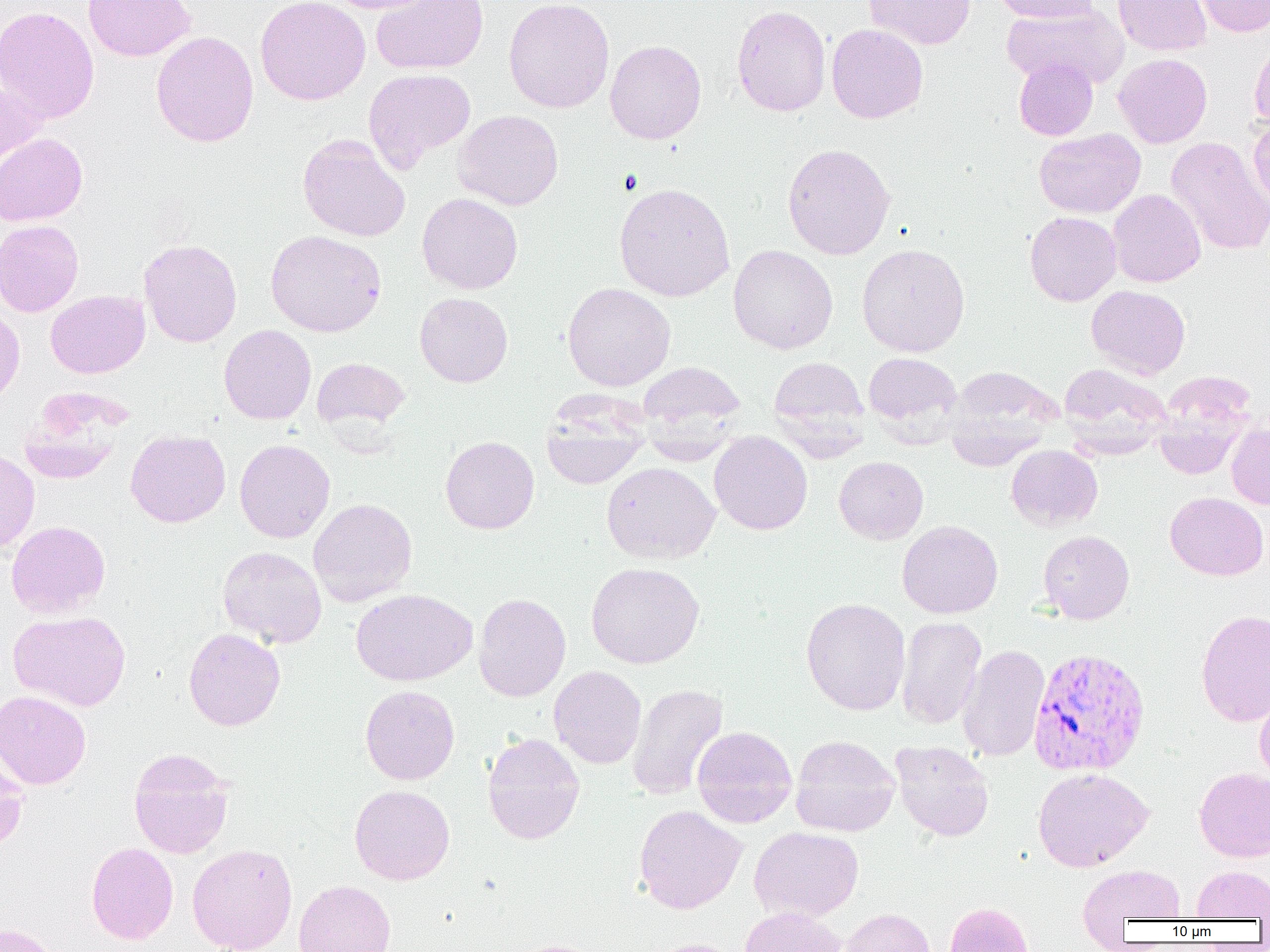

slide_level_diagnosis: Plasmodium vivax
uninfected_red_blood_cell_locations: 'approximate bounding boxes as (x1, y1, x2, y2) in pixels: (83, 0, 195, 62), (256, 0, 370, 105), (322, 0, 439, 14), (370, 0, 489, 75), (503, 0, 615, 113), (864, 0, 976, 50), (991, 0, 1099, 23), (1113, 0, 1211, 56), (1196, 0, 1269, 38), (1000, 3, 1129, 90), (732, 4, 831, 117), (0, 6, 100, 123), (826, 23, 928, 123), (151, 30, 259, 148), (1249, 37, 1270, 130), (605, 40, 706, 144), (1113, 53, 1212, 148), (1014, 57, 1098, 140), (363, 68, 476, 170), (0, 80, 46, 176), (453, 109, 564, 210), (1248, 118, 1270, 211), (1035, 128, 1146, 218), (0, 133, 87, 226), (297, 133, 411, 242), (1166, 137, 1270, 256), (782, 142, 896, 260), (613, 182, 735, 302), (1108, 189, 1206, 287), (417, 193, 523, 294), (1024, 211, 1121, 306), (0, 220, 84, 317), (265, 230, 386, 337), (138, 238, 242, 347), (857, 242, 970, 357), (728, 244, 838, 354), (562, 281, 676, 390), (1086, 284, 1191, 378), (45, 290, 150, 378), (414, 292, 513, 387), (0, 303, 25, 406), (219, 324, 316, 424), (863, 351, 962, 432), (768, 356, 869, 442), (312, 357, 410, 433), (636, 361, 745, 436), (1058, 362, 1172, 454), (944, 365, 1063, 464), (1154, 378, 1253, 479), (18, 396, 127, 486), (541, 421, 649, 490), (1226, 422, 1270, 509), (125, 429, 231, 527), (709, 432, 813, 535), (439, 438, 540, 535), (235, 439, 335, 543), (640, 442, 737, 464), (1006, 444, 1103, 531), (0, 448, 40, 554), (833, 456, 929, 544), (601, 461, 720, 564), (1165, 491, 1268, 580), (308, 498, 417, 607), (6, 520, 110, 618), (897, 520, 1003, 618), (1038, 530, 1135, 624), (217, 546, 327, 648), (586, 562, 705, 668), (351, 588, 477, 686), (473, 592, 571, 702), (801, 597, 911, 716), (1196, 609, 1270, 728), (9, 610, 131, 711), (896, 616, 987, 729), (183, 627, 286, 731), (957, 643, 1050, 762), (548, 665, 647, 769), (627, 683, 728, 800), (360, 684, 459, 785), (1, 690, 91, 789), (1255, 690, 1270, 785), (693, 725, 797, 828), (482, 732, 585, 845), (790, 735, 900, 836), (890, 740, 995, 841), (0, 745, 29, 853), (129, 748, 234, 858), (1033, 767, 1153, 872), (1194, 768, 1270, 862), (349, 784, 455, 885), (634, 804, 747, 913), (750, 826, 864, 921), (86, 842, 178, 944), (187, 843, 297, 952), (1078, 865, 1186, 923), (1191, 866, 1270, 920), (293, 880, 396, 952), (945, 902, 1033, 952), (740, 906, 847, 952), (839, 908, 935, 952), (0, 922, 60, 952), (644, 938, 746, 952), (511, 939, 608, 952)'
plasmodium_vivax_infected_red_blood_cell_locations: 'approximate bounding boxes as (x1, y1, x2, y2) in pixels: (1027, 646, 1151, 777)'
preparation: thin blood smear
field_of_view: one of a larger specimen
magnification: 1000x
modality: optical microscopy
image_size: 1270×952 pixels